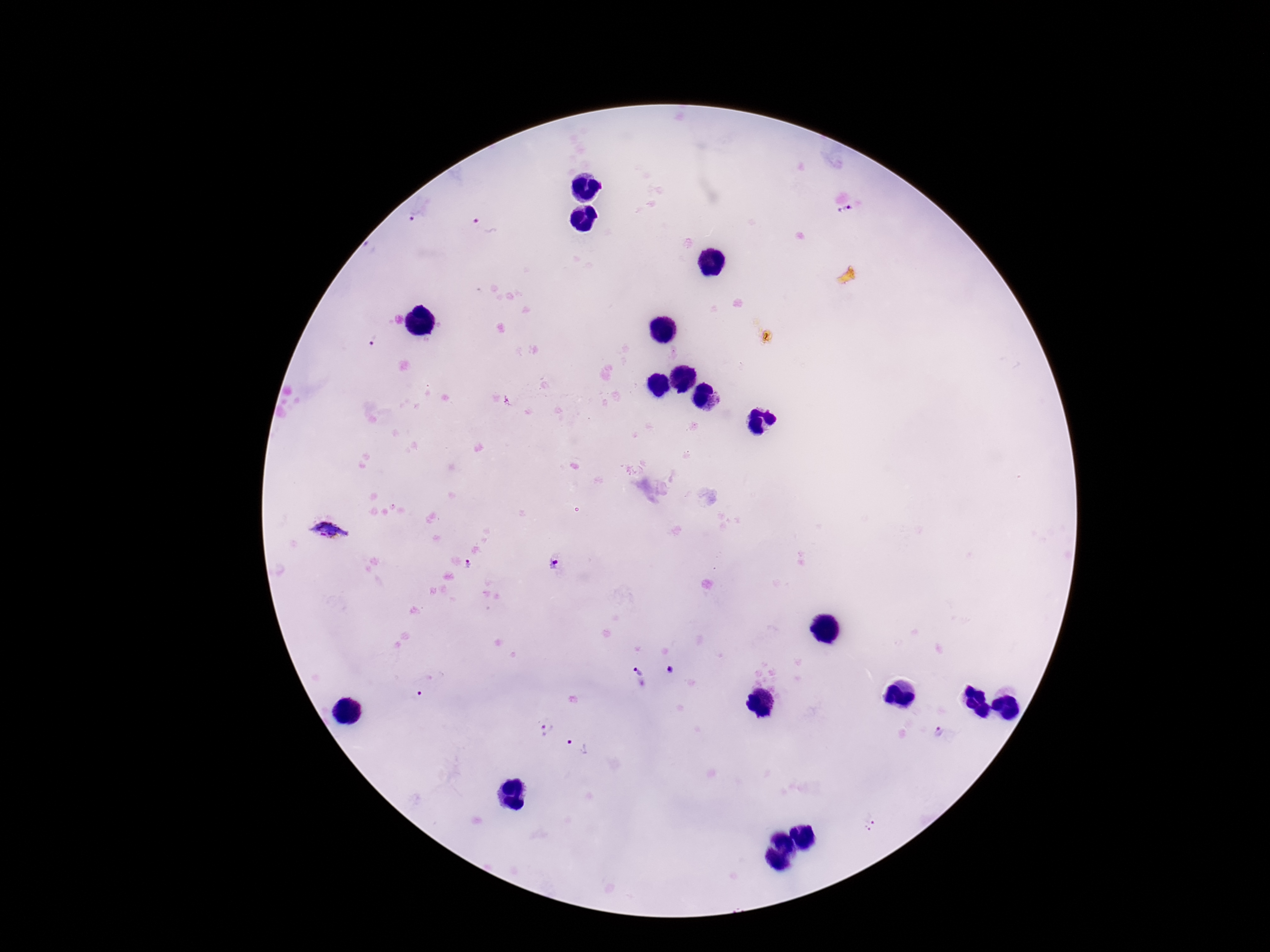

field_of_view: single
patient_malaria_status: infected
capture: smartphone camera through the microscope eyepiece
plasmodium_parasite_locations: 'approximate centers as {x, y} in pixels: {844, 213}, {414, 217}, {484, 223}, {374, 340}, {328, 532}, {554, 561}, {469, 564}, {638, 666}, {670, 670}, {426, 686}, {544, 728}, {938, 732}, {575, 745}, {870, 823}'
preparation: thick blood film
magnification: 100x
stain: Giemsa
image_size: 1270×952 pixels